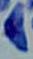
magnification = 1000x
modality = micrograph
identification = Toxoplasma gondii